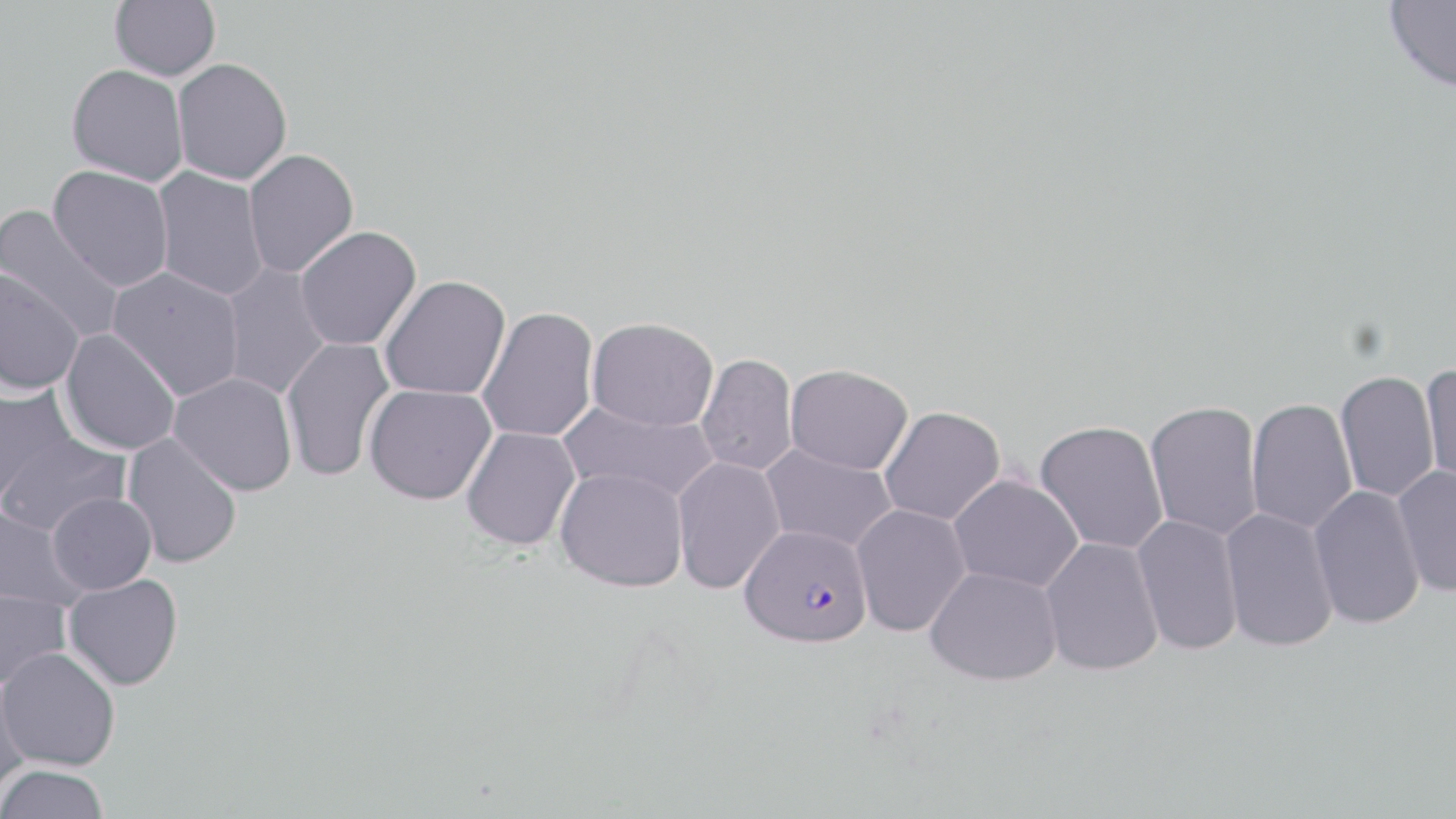

Approximate bounding boxes as (x1, y1, x2, y2) in pixels. Uninfected red blood cell locations: (110, 0, 220, 81), (1383, 0, 1456, 92), (172, 58, 292, 186), (66, 64, 189, 186), (243, 149, 359, 278), (48, 165, 174, 292), (152, 167, 269, 301), (0, 204, 126, 345), (294, 226, 421, 352), (219, 262, 332, 401), (107, 268, 244, 401), (0, 269, 84, 396), (379, 275, 511, 401), (477, 306, 599, 443), (586, 317, 718, 431), (59, 329, 181, 456), (280, 336, 396, 483), (696, 353, 798, 476), (784, 364, 913, 475), (1420, 365, 1456, 494), (1335, 371, 1440, 504), (167, 372, 298, 497), (0, 382, 79, 503), (363, 384, 496, 505), (1246, 397, 1357, 534), (558, 400, 718, 504), (1144, 400, 1263, 541), (878, 406, 1005, 526), (1034, 420, 1168, 556), (460, 427, 580, 551), (121, 432, 243, 569), (0, 433, 131, 537), (760, 445, 898, 553), (672, 456, 785, 595), (1392, 466, 1456, 598), (555, 467, 689, 592), (948, 475, 1083, 591), (1308, 485, 1425, 630), (47, 492, 157, 594), (850, 503, 970, 637), (0, 504, 88, 611), (1219, 507, 1338, 653), (1132, 515, 1243, 657), (1039, 538, 1163, 676), (924, 566, 1063, 686), (63, 574, 183, 690), (0, 588, 71, 691), (1, 646, 121, 771), (0, 671, 32, 799), (0, 764, 110, 819). Plasmodium falciparum-infected red blood cell locations: (740, 524, 873, 647). Slide-level diagnosis: Plasmodium falciparum. Captured at 1000x magnification. Image is 1456×819 pixels. One field of a larger specimen. Thin blood smear. May-Grünwald-Giemsa stain. Optical microscopy.